Outline each Plasmodium vivax-infected red blood cell.
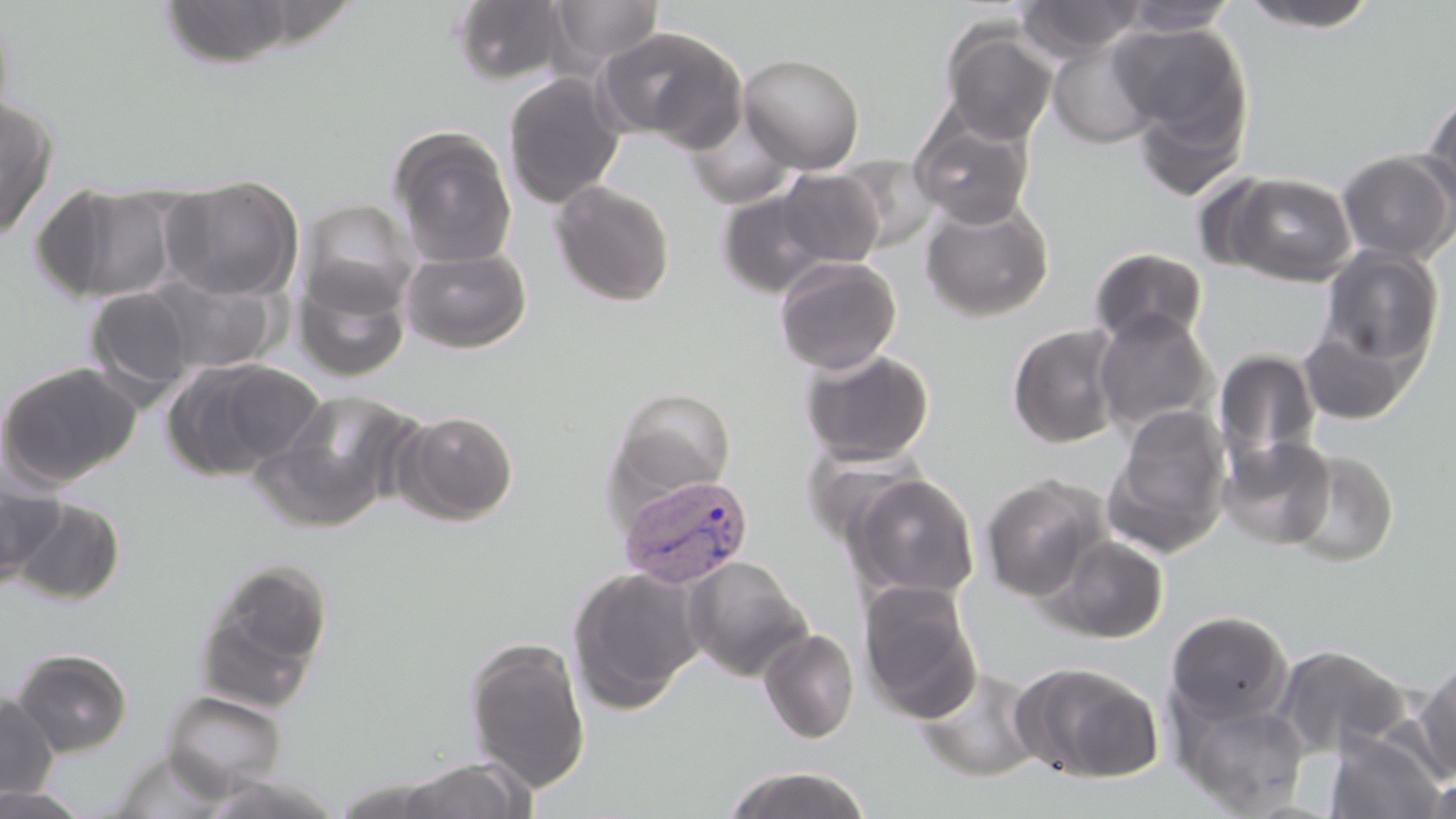

Approximate bounding boxes as (x1, y1, x2, y2) in pixels.
Plasmodium vivax-infected red blood cells: (617, 471, 757, 588).

{
  "slide_level_diagnosis": "Plasmodium vivax",
  "uninfected_red_blood_cell_locations": "approximate bounding boxes as (x1, y1, x2, y2) in pixels: (450, 0, 570, 85), (1017, 0, 1146, 62), (156, 1, 303, 68), (548, 1, 665, 72), (1120, 1, 1241, 36), (1234, 1, 1384, 32), (0, 2, 16, 139), (1113, 22, 1251, 144), (941, 23, 1059, 144), (595, 25, 747, 149), (1046, 36, 1163, 148), (738, 52, 865, 174), (503, 72, 625, 208), (1131, 88, 1249, 202), (1423, 90, 1456, 209), (0, 94, 60, 238), (684, 114, 797, 209), (911, 115, 1034, 228), (389, 128, 518, 268), (1337, 149, 1456, 264), (836, 154, 940, 252), (777, 168, 884, 267), (1226, 172, 1357, 286), (161, 175, 302, 302), (551, 180, 675, 306), (32, 182, 179, 304), (716, 186, 834, 298), (919, 196, 1054, 321), (298, 198, 421, 316), (401, 246, 532, 353), (1319, 247, 1444, 371), (1089, 248, 1208, 347), (774, 255, 902, 374), (294, 269, 410, 381), (143, 272, 280, 376), (85, 287, 201, 399), (1093, 309, 1216, 434), (1006, 323, 1127, 449), (1296, 329, 1414, 425), (800, 346, 935, 465), (1212, 348, 1323, 471), (160, 357, 320, 481), (0, 361, 142, 489), (252, 388, 420, 532), (609, 389, 738, 500), (1105, 404, 1232, 556), (394, 410, 519, 525), (1219, 435, 1337, 549), (1285, 448, 1400, 568), (0, 463, 66, 587), (846, 473, 980, 600), (980, 475, 1106, 601), (8, 496, 126, 605), (1044, 534, 1170, 644), (194, 556, 333, 711), (683, 557, 814, 681), (568, 566, 706, 712), (858, 581, 982, 720), (1166, 610, 1293, 728), (759, 628, 859, 743), (463, 637, 592, 794), (1273, 644, 1408, 759), (10, 646, 133, 757), (1415, 659, 1456, 779), (1014, 661, 1164, 784), (915, 666, 1046, 782), (162, 689, 288, 798), (0, 693, 59, 803), (1176, 698, 1310, 816), (1324, 732, 1445, 817), (109, 749, 230, 818), (393, 757, 535, 819), (722, 766, 873, 818), (329, 775, 465, 817), (198, 776, 344, 819), (1422, 776, 1456, 818), (0, 783, 94, 818)",
  "modality": "optical microscopy",
  "stain": "May-Grünwald-Giemsa",
  "image_size": "1456×819 pixels",
  "field_of_view": "single",
  "magnification": "1000x",
  "preparation": "thin blood film"
}